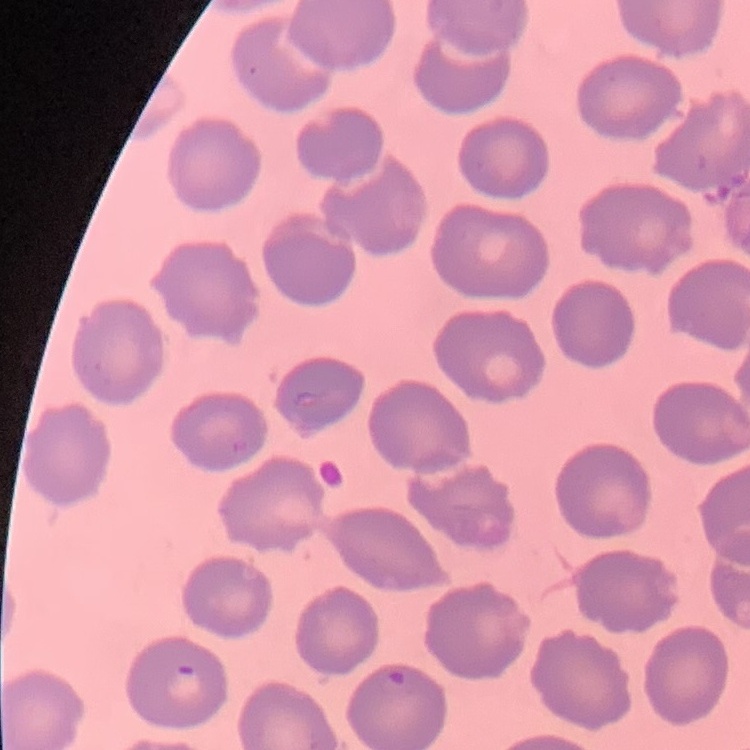

erythrocyte morphology = no rouleaux formation
stain = Field's or Giemsa
preparation = thin blood smear
image type = one tile cut from a larger photomicrograph